Point out each Plasmodium parasite.
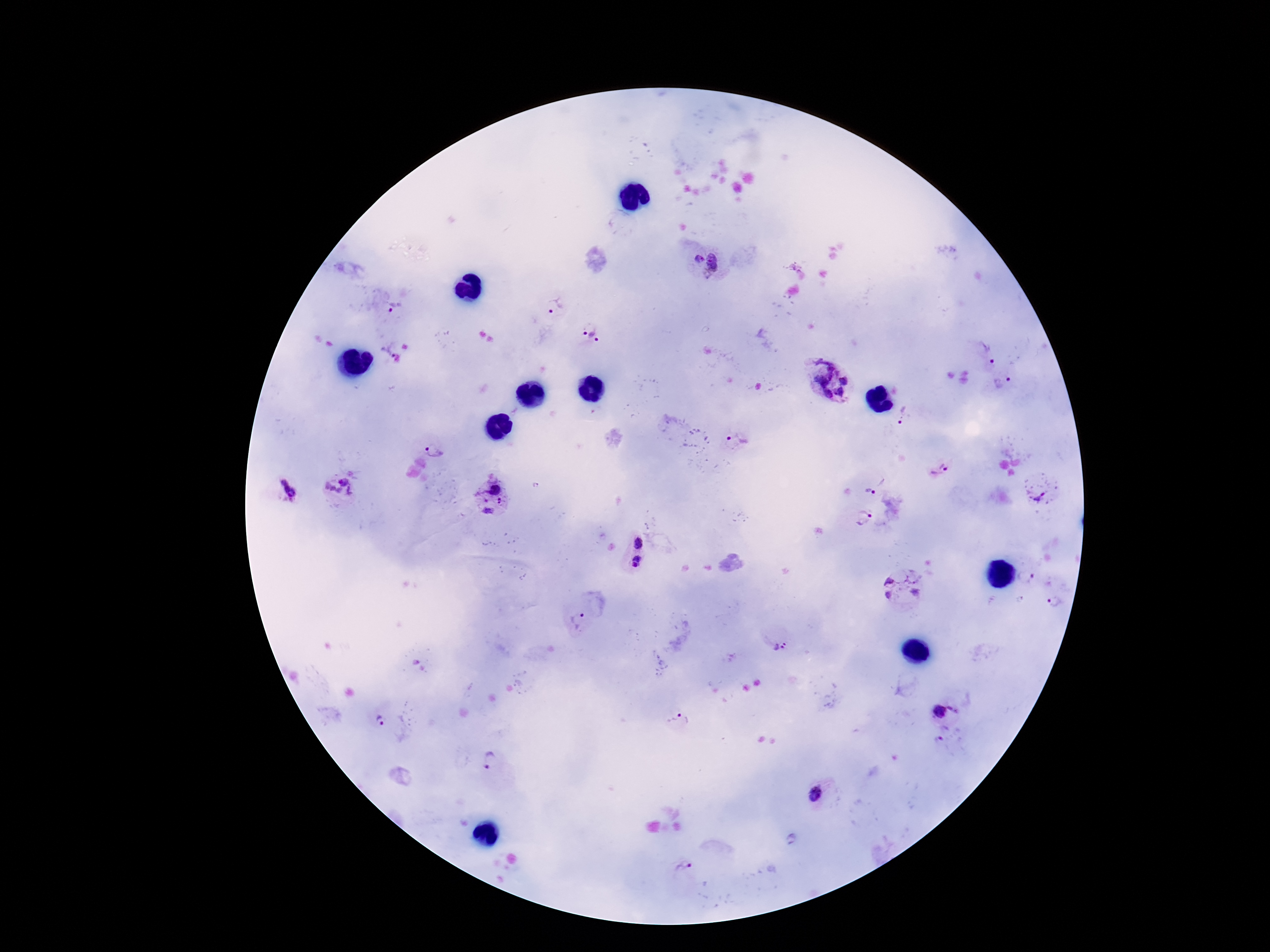
Approximate object centers, in pixels from the top-left corner.
Plasmodium parasites: (x=697, y=258), (x=719, y=262), (x=394, y=305), (x=554, y=305), (x=590, y=332), (x=384, y=348), (x=987, y=350), (x=829, y=380), (x=1003, y=383), (x=903, y=417), (x=735, y=442), (x=435, y=448), (x=938, y=469), (x=493, y=485), (x=288, y=490), (x=340, y=490), (x=1039, y=491), (x=869, y=492), (x=501, y=502), (x=488, y=511), (x=864, y=520), (x=638, y=542), (x=637, y=562), (x=1027, y=577), (x=901, y=586), (x=1057, y=603), (x=576, y=621), (x=780, y=647), (x=955, y=709), (x=939, y=711), (x=381, y=720), (x=678, y=721), (x=491, y=761), (x=816, y=796), (x=684, y=865).

magnification = 100x
preparation = thick blood film
field of view = single
stain = Giemsa
capture = smartphone camera through the microscope eyepiece
image size = 1270×952 pixels
patient malaria status = positive